Classify this cell by malaria status.
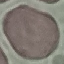

Uninfected.

Summary:
  - Stain: Giemsa
  - Capture: smartphone through the microscope eyepiece
  - Image type: cell patch, automatically extracted from a larger field of view and resized to 64 × 64 pixels
  - Preparation: thin blood film